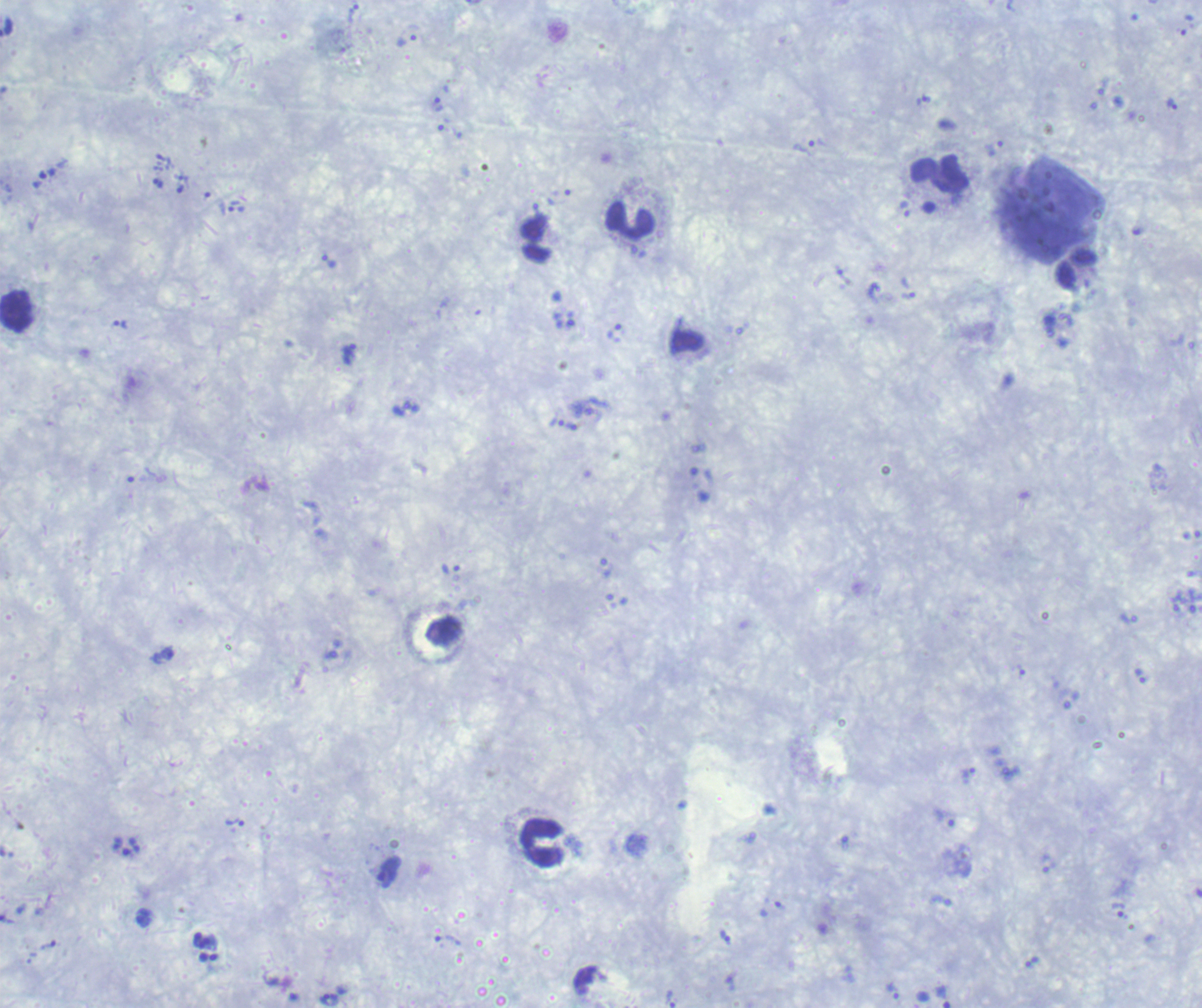
coordinate format = approximate centers as [x, y] in pixels
gametocyte locations = [388, 872]
leukocyte locations = [939, 175], [630, 220], [1077, 270], [17, 312], [543, 843]
trophozoite locations = [407, 40], [924, 101], [438, 104], [1171, 105], [805, 148], [994, 148], [158, 183], [236, 209], [329, 261], [121, 325], [348, 354], [556, 423], [452, 569], [1141, 677], [968, 773], [234, 822], [1119, 910], [726, 937], [1032, 962], [893, 992], [671, 999], [329, 1000]
life-cycle stages observed = trophozoite, gametocyte
preparation = thick blood smear
stain = Romanowsky
background quality = unsatisfactory
image size = 1202×1008 pixels
context = previously used in an actual diagnosis
magnification = 100x
result = positive for malaria parasites
field of view = single